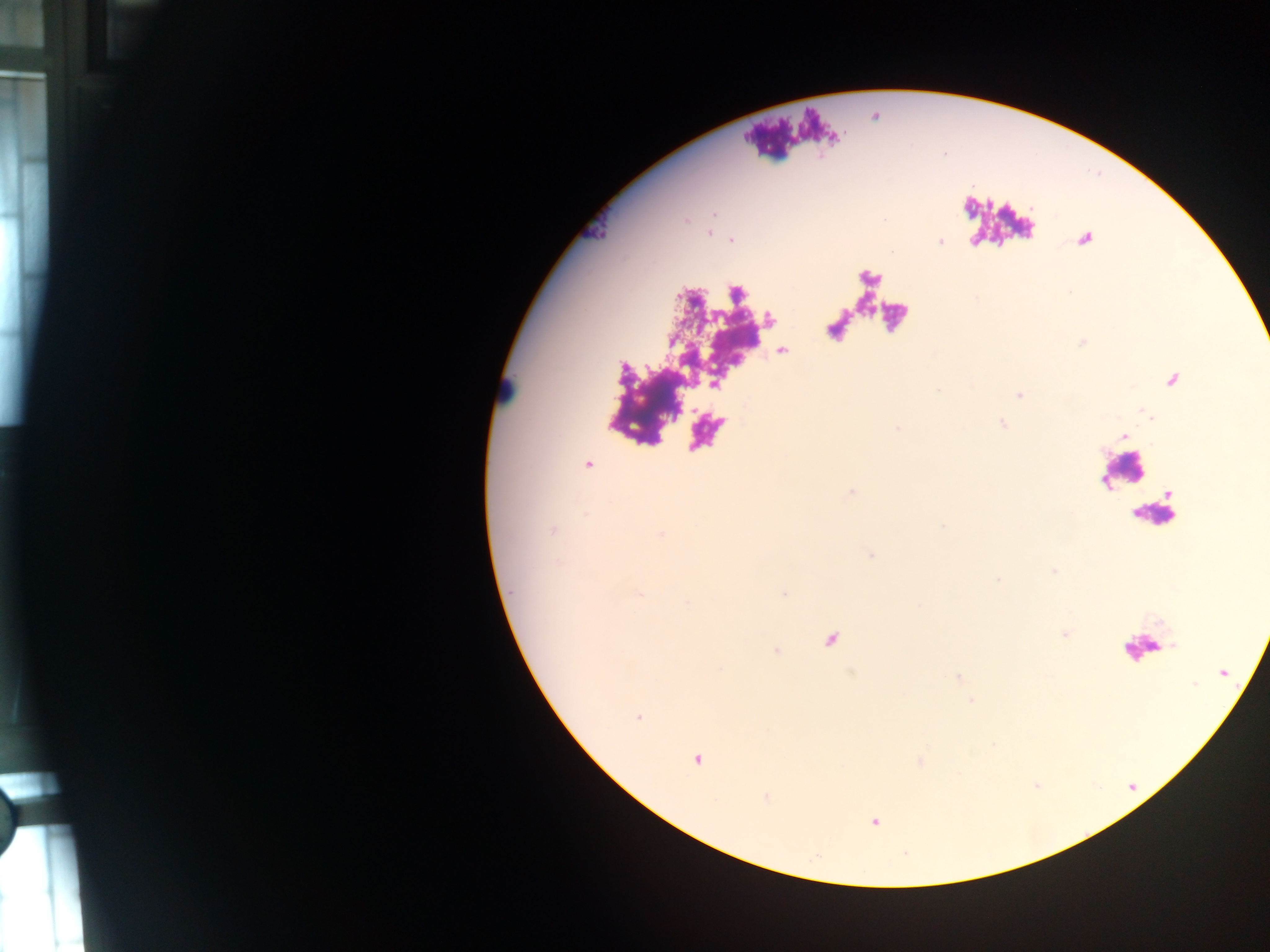

image size = 1270×952 pixels
leukocyte locations = approximate centers as [x, y] in pixels: [505, 392], [1122, 471], [1156, 514], [1142, 648]
Plasmodium parasite locations = approximate centers as [x, y] in pixels: [710, 232], [731, 240], [1019, 393], [588, 465], [660, 534], [830, 639], [957, 677], [971, 701], [638, 717], [695, 758], [919, 760], [766, 798], [873, 820]
preparation = thick blood film
field of view = single
capture = mobile-phone photograph through a microscope
country = Ghana